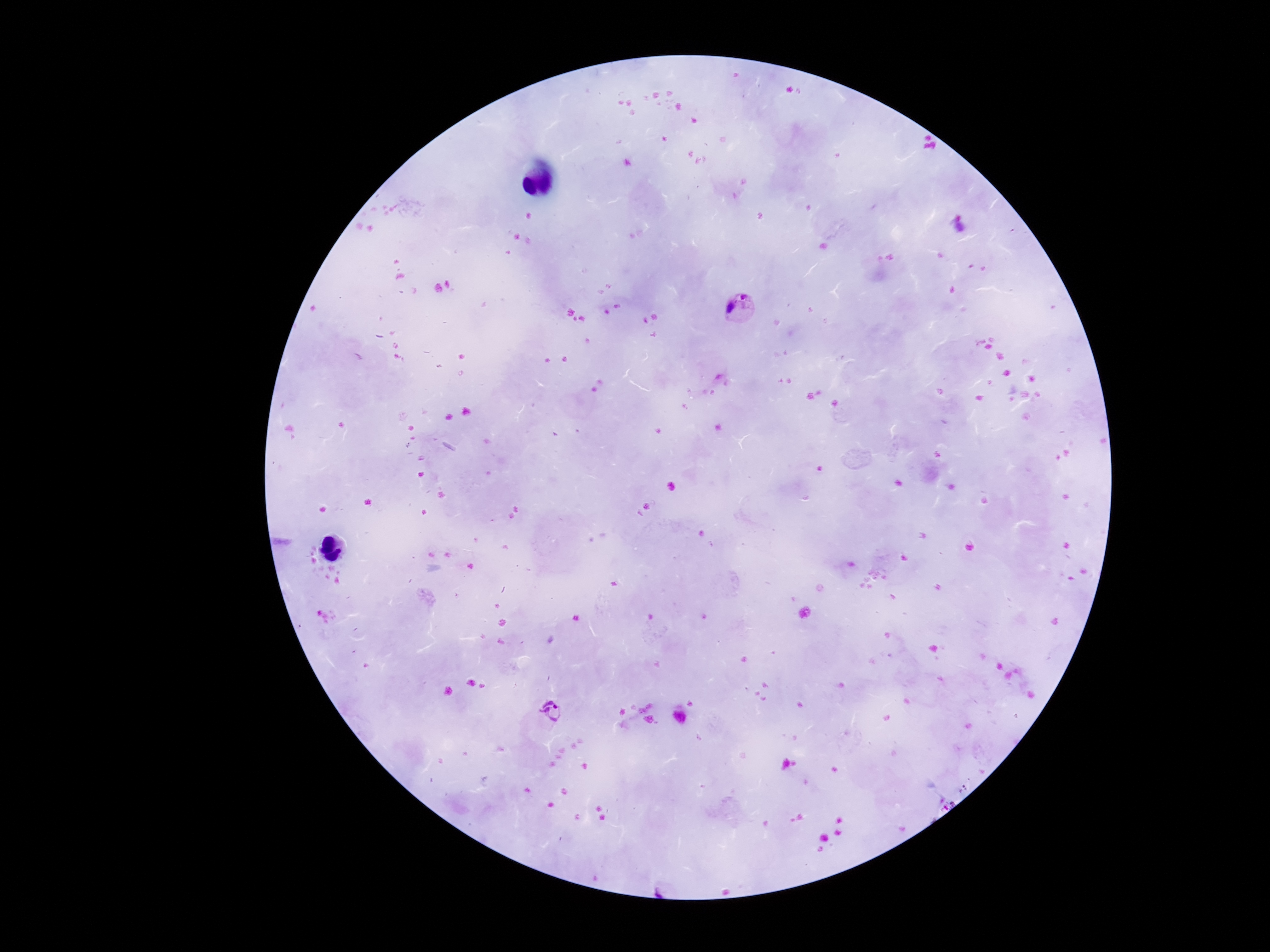

{
  "image_size": "1270×952 pixels",
  "preparation": "thick peripheral-blood smear",
  "patient_malaria_status": "positive",
  "plasmodium_parasite_locations": "approximate centers as [x, y] in pixels: [740, 312], [549, 712]",
  "field_of_view": "one from this slide",
  "capture": "smartphone camera through the microscope eyepiece",
  "stain": "Giemsa",
  "magnification": "100x"
}